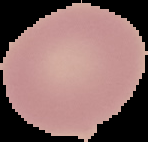

image type = cell region segmented out of the field of view; surrounding area masked to black
preparation = thin blood film
image size = 148×142 pixels
malaria status = uninfected